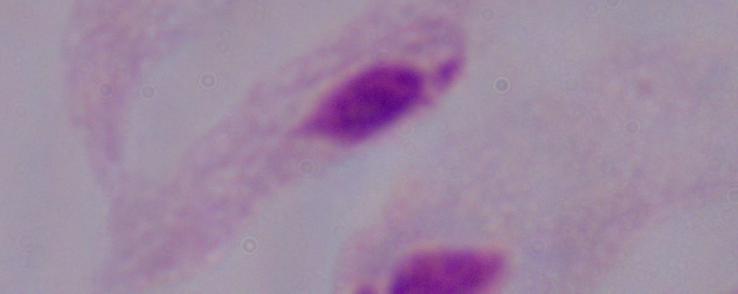

Summary:
  - Magnification: 1000x
  - Modality: micrograph
  - Identification: trichomonad